Locate every Plasmodium ovale-infected red blood cell.
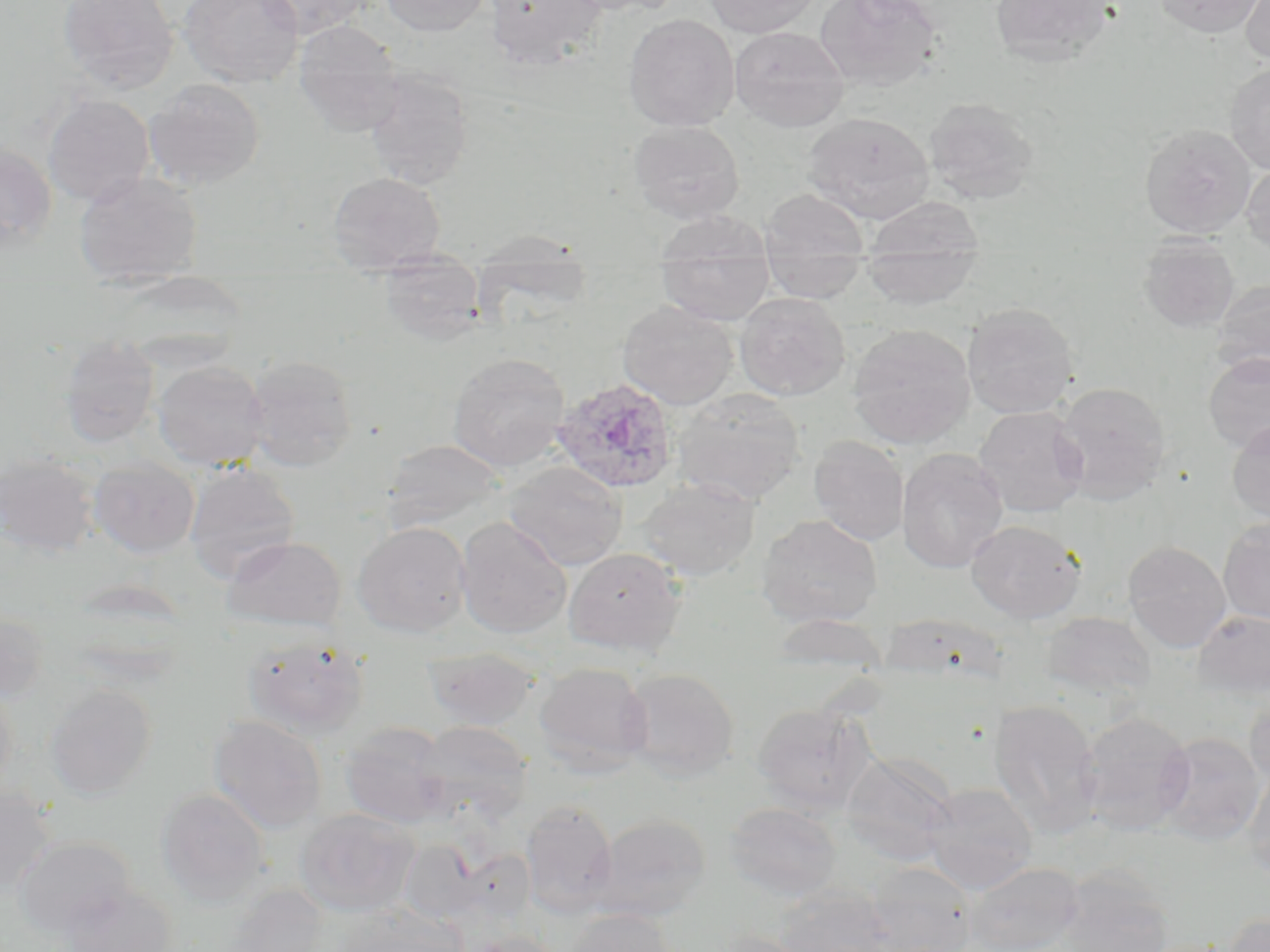

Approximate bounding boxes as (x1, y1, x2, y2) in pixels.
Plasmodium ovale-infected red blood cells: (551, 377, 679, 494).

Uninfected red blood cell locations: (57, 0, 179, 93), (178, 0, 304, 87), (257, 0, 373, 38), (380, 0, 492, 36), (483, 0, 607, 69), (562, 0, 687, 16), (704, 0, 820, 37), (815, 0, 942, 92), (989, 0, 1118, 66), (1154, 0, 1266, 38), (1239, 0, 1270, 66), (623, 14, 740, 131), (292, 21, 405, 137), (729, 26, 849, 131), (1224, 62, 1270, 174), (363, 70, 474, 190), (144, 78, 266, 190), (42, 93, 155, 206), (923, 97, 1040, 204), (803, 112, 934, 224), (627, 120, 745, 224), (1140, 124, 1256, 238), (0, 141, 57, 249), (1241, 160, 1270, 257), (73, 171, 203, 279), (327, 172, 446, 271), (760, 188, 869, 260), (864, 199, 983, 275), (651, 211, 774, 263), (469, 229, 591, 264), (1138, 234, 1239, 333), (860, 241, 983, 309), (763, 256, 866, 303), (657, 260, 775, 325), (376, 265, 489, 344), (472, 265, 597, 313), (107, 276, 251, 346), (1211, 278, 1270, 380), (734, 292, 850, 401), (617, 300, 738, 410), (962, 302, 1079, 419), (847, 324, 976, 449), (59, 336, 159, 446), (1202, 352, 1270, 453), (447, 353, 570, 472), (246, 355, 359, 471), (152, 361, 269, 470), (1054, 381, 1170, 503), (672, 388, 806, 505), (973, 406, 1089, 517), (1226, 419, 1270, 528), (809, 436, 909, 546), (382, 439, 506, 530), (897, 448, 1009, 573), (0, 452, 100, 556), (88, 456, 200, 558), (504, 461, 628, 570), (184, 463, 300, 583), (637, 476, 760, 581), (757, 514, 883, 628), (455, 517, 572, 638), (1217, 519, 1270, 625), (966, 520, 1086, 623), (353, 521, 472, 636), (220, 536, 347, 630), (1122, 539, 1232, 653), (564, 547, 687, 657), (1193, 609, 1270, 698), (0, 611, 50, 702), (1041, 612, 1156, 701), (767, 613, 893, 679), (241, 634, 370, 738), (423, 647, 541, 731), (534, 663, 653, 773), (620, 667, 739, 780), (0, 679, 17, 801), (44, 684, 157, 799), (1244, 693, 1270, 794), (989, 699, 1103, 838), (751, 703, 874, 813), (1078, 710, 1195, 835), (208, 715, 328, 834), (414, 721, 533, 822), (339, 722, 451, 829), (1154, 731, 1266, 844), (841, 751, 956, 866), (1242, 764, 1270, 883), (921, 781, 1038, 893), (0, 786, 56, 893), (155, 788, 271, 908), (520, 800, 618, 917), (724, 802, 842, 901), (295, 808, 420, 917), (593, 814, 711, 921), (13, 836, 135, 935), (398, 839, 484, 925), (454, 848, 536, 926), (965, 861, 1084, 952), (863, 863, 978, 951), (1058, 868, 1175, 952), (56, 882, 179, 952), (220, 884, 331, 952), (773, 885, 896, 952), (330, 903, 466, 952), (564, 907, 677, 952), (1221, 910, 1270, 952), (710, 929, 818, 952), (464, 931, 565, 952). Slide-level diagnosis: Plasmodium ovale. Captured at 1000x magnification. May-Grünwald-Giemsa stain. Thin blood smear. Single field of view. Light microscopy. Image is 1270×952 pixels.